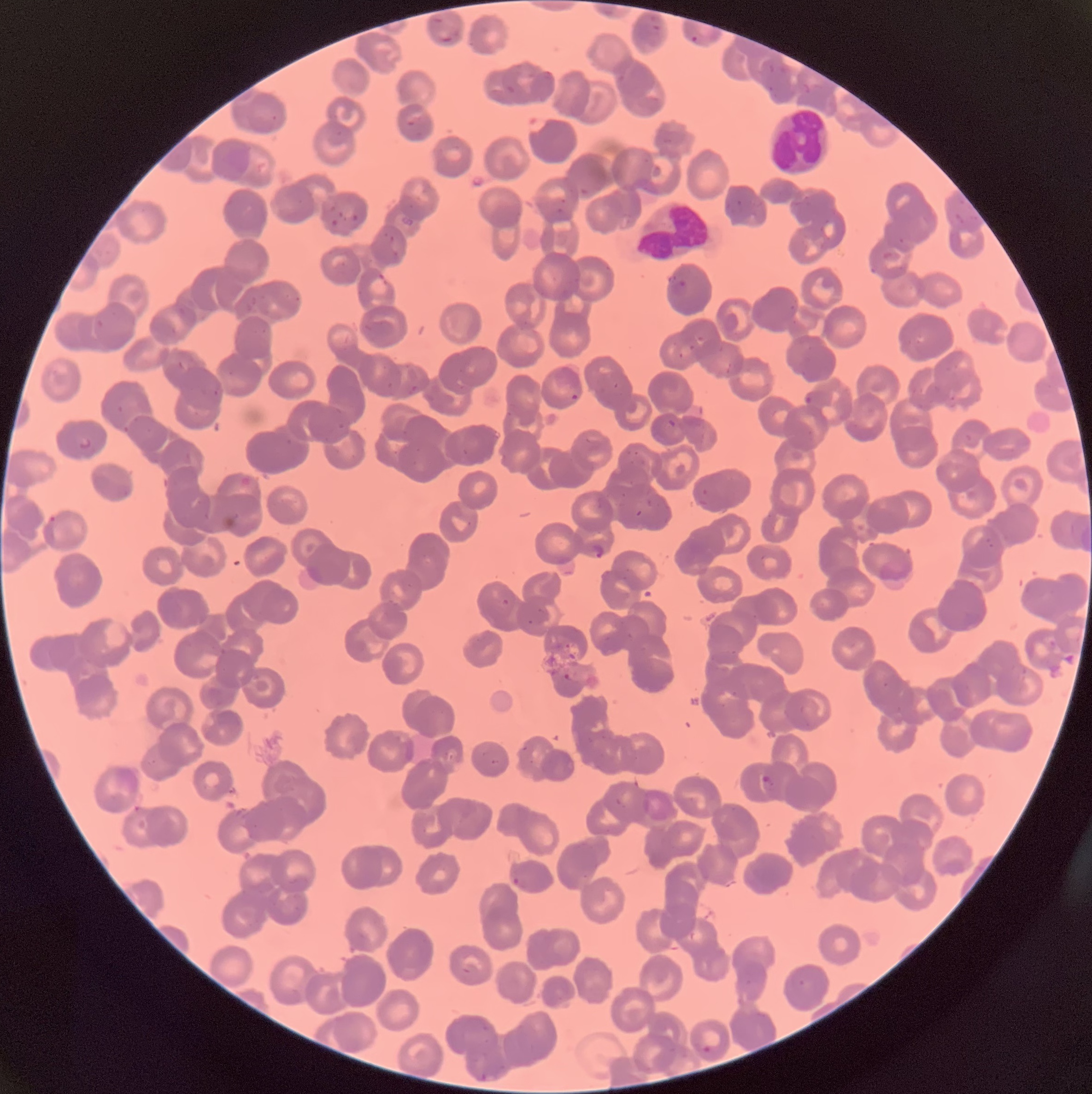
coordinate format = approximate bounding boxes as (x1,y1)-(x2,y2) corner pairs in pixels
Plasmodium parasite locations = (690,34)-(699,44), (670,278)-(688,298), (569,393)-(579,403), (667,418)-(676,428), (78,438)-(94,451), (590,542)-(607,560), (563,673)-(580,683), (761,775)-(774,791), (512,876)-(529,888), (702,1043)-(714,1056), (474,1070)-(496,1081)
white blood cell locations = (768,107)-(832,178), (637,197)-(707,264)
image size = 1092×1094 pixels
modality = light microscopy
preparation = thin blood film
red blood cell morphology = rouleaux formation